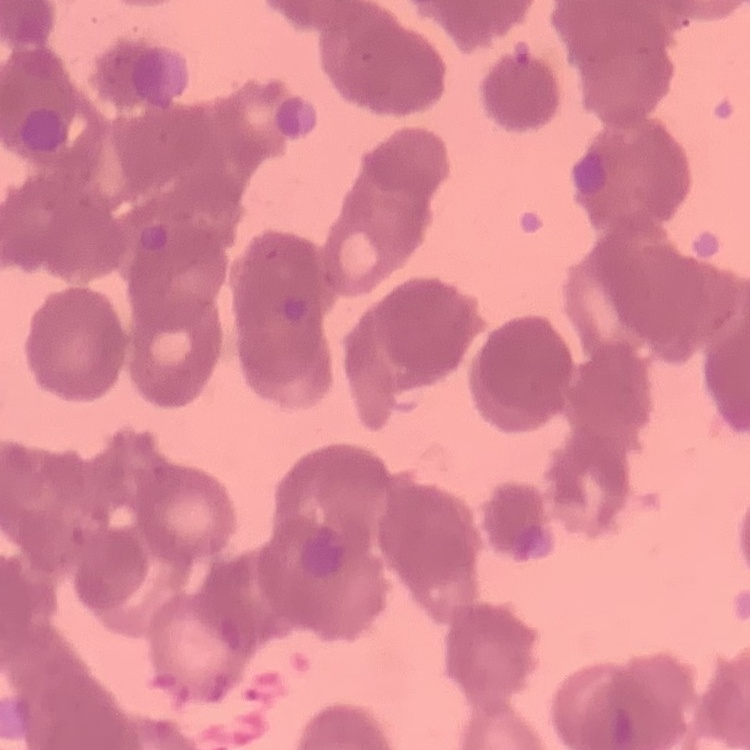 The red blood cells show rouleaux formation. Thin blood film. One tile cut from a larger photomicrograph. Stained with either Field's or Giemsa.